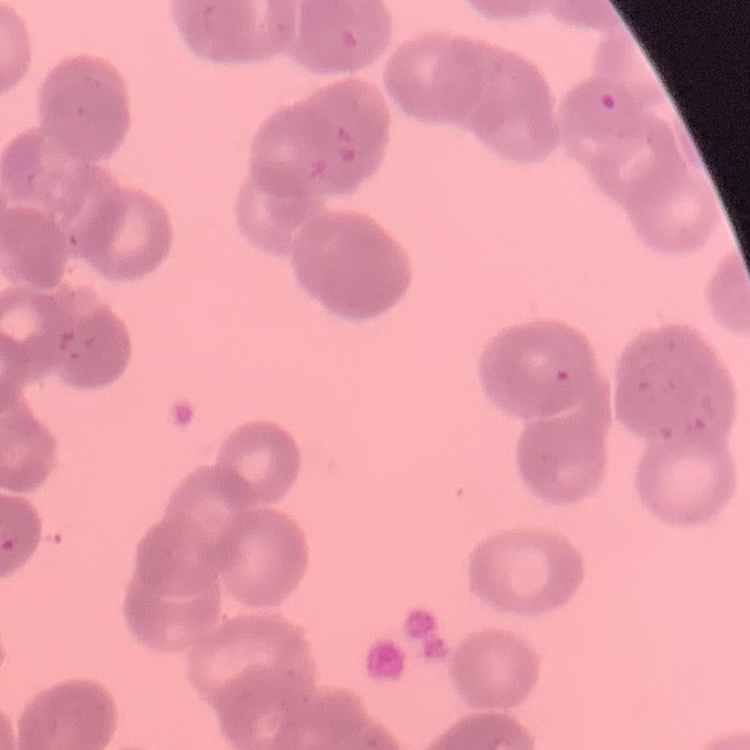

Summary:
  - Red blood cell morphology: rouleaux formation
  - Image type: square crop of a larger photomicrograph
  - Preparation: thin blood film
  - Stain: Field's or Giemsa